Locate and identify every blood parasite.
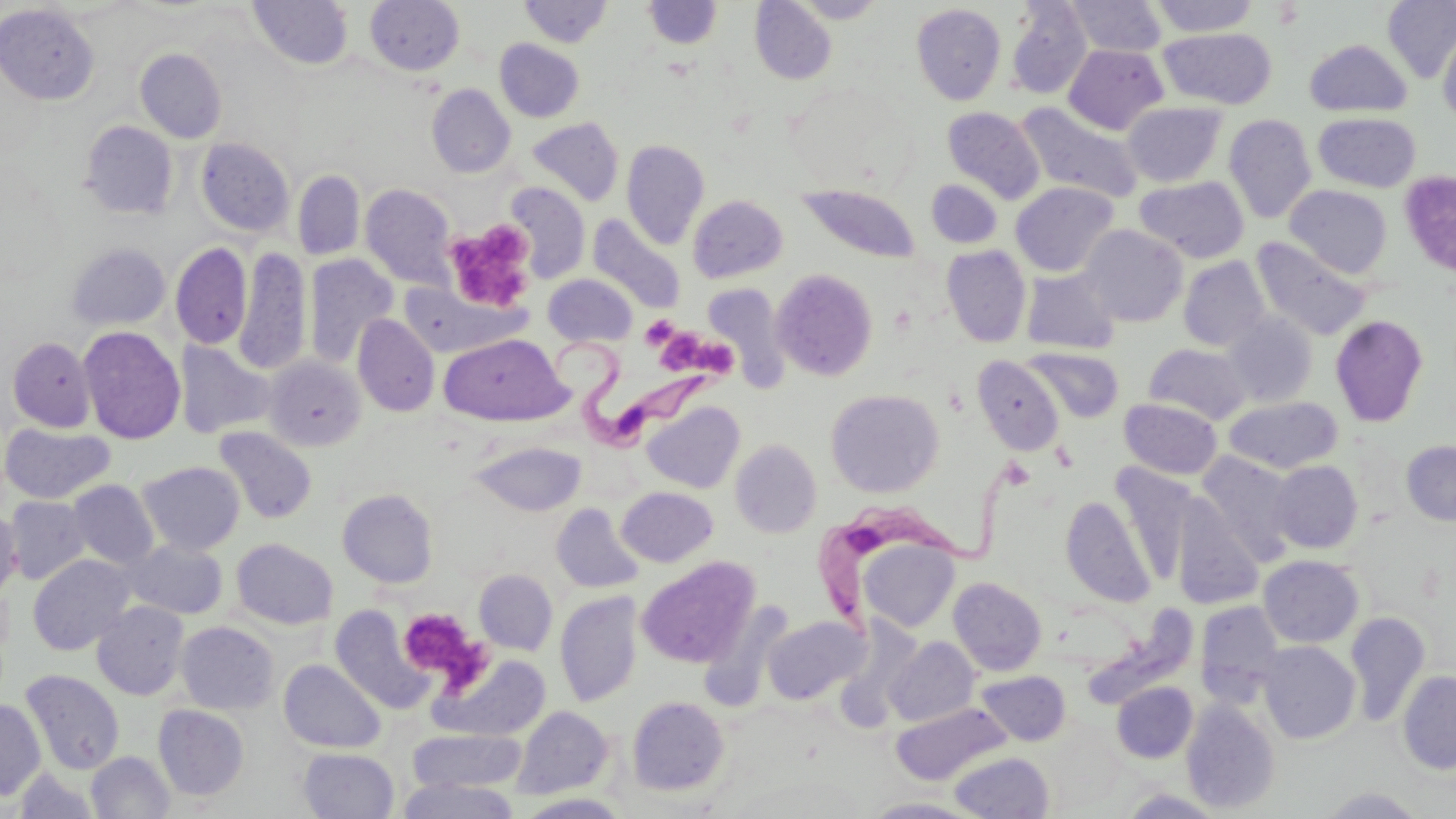
Approximate bounding boxes as [x1, y1, x2, y2] in pixels.
Trypanosoma brucei: [539, 340, 728, 463], [808, 467, 1030, 628].
No Plasmodium falciparum, Plasmodium ovale, Plasmodium malariae, Plasmodium vivax, or Babesia divergens observed.

Uninfected red blood cell locations: [365, 0, 465, 76], [790, 0, 889, 23], [1066, 0, 1167, 57], [1149, 0, 1259, 36], [1383, 0, 1456, 83], [247, 1, 353, 70], [520, 1, 613, 47], [643, 1, 723, 48], [749, 1, 837, 85], [911, 3, 1007, 105], [1005, 3, 1092, 99], [0, 4, 99, 105], [1438, 25, 1456, 127], [1159, 28, 1276, 109], [495, 39, 584, 122], [1304, 39, 1413, 117], [1063, 44, 1168, 134], [135, 48, 227, 143], [426, 84, 516, 178], [1122, 101, 1227, 187], [1015, 102, 1143, 203], [942, 107, 1045, 203], [1313, 112, 1421, 193], [1224, 114, 1317, 223], [527, 117, 624, 206], [80, 121, 178, 219], [196, 137, 295, 236], [621, 139, 709, 249], [292, 170, 365, 260], [1135, 175, 1249, 263], [927, 180, 1002, 248], [505, 181, 590, 284], [1011, 182, 1118, 277], [360, 184, 457, 289], [796, 184, 921, 264], [1285, 185, 1393, 278], [688, 195, 788, 283], [587, 215, 687, 314], [1081, 224, 1188, 327], [1251, 236, 1372, 340], [65, 242, 171, 331], [170, 242, 252, 349], [942, 245, 1032, 347], [234, 247, 311, 375], [303, 254, 399, 367], [1178, 256, 1270, 351], [1021, 268, 1120, 354], [771, 269, 878, 381], [543, 274, 637, 346], [399, 283, 528, 358], [703, 285, 792, 388], [1222, 311, 1317, 407], [352, 314, 440, 416], [1330, 314, 1428, 426], [78, 326, 186, 444], [439, 334, 569, 425], [7, 336, 96, 431], [174, 339, 276, 439], [1144, 343, 1252, 425], [1023, 347, 1124, 422], [264, 355, 365, 452], [971, 355, 1065, 456], [826, 388, 943, 497], [1119, 397, 1222, 480], [1224, 397, 1342, 473], [642, 401, 745, 493], [0, 422, 114, 504], [213, 427, 317, 524], [730, 439, 822, 538], [470, 440, 586, 516], [1401, 440, 1456, 525], [1197, 452, 1299, 564], [1269, 460, 1363, 553], [137, 461, 245, 555], [1109, 462, 1197, 587], [67, 479, 159, 569], [616, 487, 718, 567], [337, 488, 438, 588], [4, 496, 91, 584], [1061, 496, 1155, 607], [1171, 497, 1262, 609], [551, 503, 644, 594], [0, 509, 22, 600], [231, 538, 338, 629], [857, 539, 959, 633], [125, 540, 228, 619], [27, 554, 135, 655], [1258, 555, 1364, 648], [637, 556, 759, 668], [474, 570, 558, 655], [949, 576, 1047, 676], [555, 592, 642, 707], [92, 601, 190, 700], [1194, 601, 1286, 707], [331, 605, 434, 714], [1080, 607, 1200, 709], [1345, 611, 1431, 727], [763, 614, 868, 704], [176, 621, 279, 715], [885, 637, 979, 726], [1258, 640, 1361, 744], [430, 653, 551, 742], [278, 659, 386, 753], [21, 669, 125, 775], [1397, 670, 1456, 774], [977, 671, 1070, 745], [1111, 681, 1198, 763], [627, 696, 729, 796], [0, 699, 46, 800], [1182, 699, 1280, 814], [891, 702, 1011, 785], [153, 705, 249, 800], [511, 706, 613, 800], [408, 729, 526, 792], [298, 747, 399, 819], [86, 751, 174, 818], [949, 752, 1054, 819], [13, 767, 101, 818], [396, 778, 520, 819], [1318, 786, 1429, 818], [1119, 789, 1229, 818], [517, 793, 632, 818], [862, 797, 982, 818]. Platelet locations: [442, 221, 538, 312], [640, 316, 680, 349], [665, 332, 708, 379], [708, 341, 741, 375], [398, 606, 482, 682]. Slide-level diagnosis: Trypanosoma brucei. May-Grünwald-Giemsa-stained preparation. Thin blood film. 1000x magnification. Image is 1456×819 pixels. One field of a larger specimen. Light microscopy.